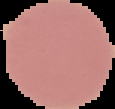
malaria_status: uninfected
image_size: 115×109 pixels
preparation: thin blood smear
image_type: segmented cell region on a black background